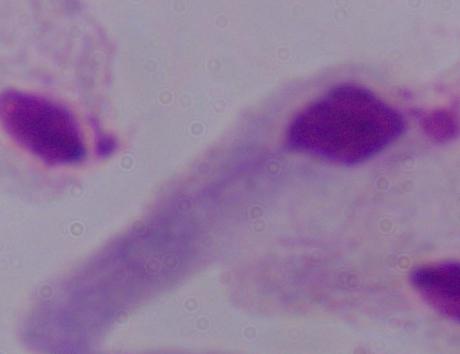
magnification: 1000x
identification: trichomonad
modality: photomicrograph